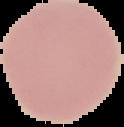
preparation = thin blood smear
result = negative for malaria parasites
image size = 124×127 pixels
image type = cell region segmented out of the field of view; surrounding area masked to black